Evaluate for Plasmodium parasites.
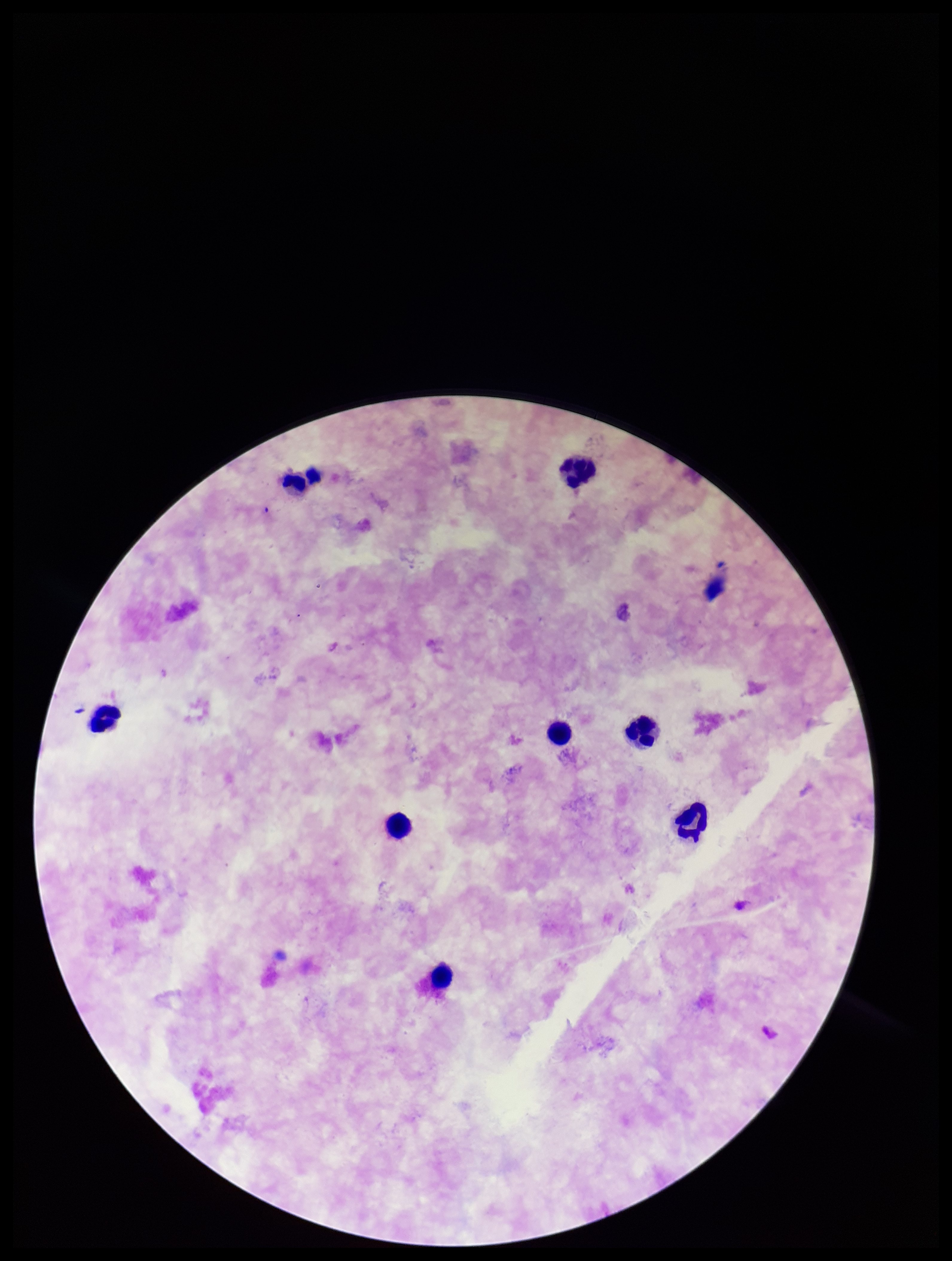

None seen.

Image is 952×1261 pixels. Stained with Giemsa. Single field of view. Parasite count: 0. Patient malaria status: negative. Preparation: thick. Leukocyte count: 8. Smartphone photograph taken through the eyepiece of a microscope.